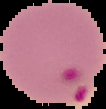

Summary:
  - Preparation: thin blood smear
  - Image type: cell region segmented out of the field of view; surrounding area masked to black
  - Result: Plasmodium parasites identified
  - Image size: 106×109 pixels